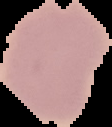

image_size: 112×127 pixels
image_type: cell region segmented out of the field of view; surrounding area masked to black
result: no malaria parasites detected
preparation: thin blood film